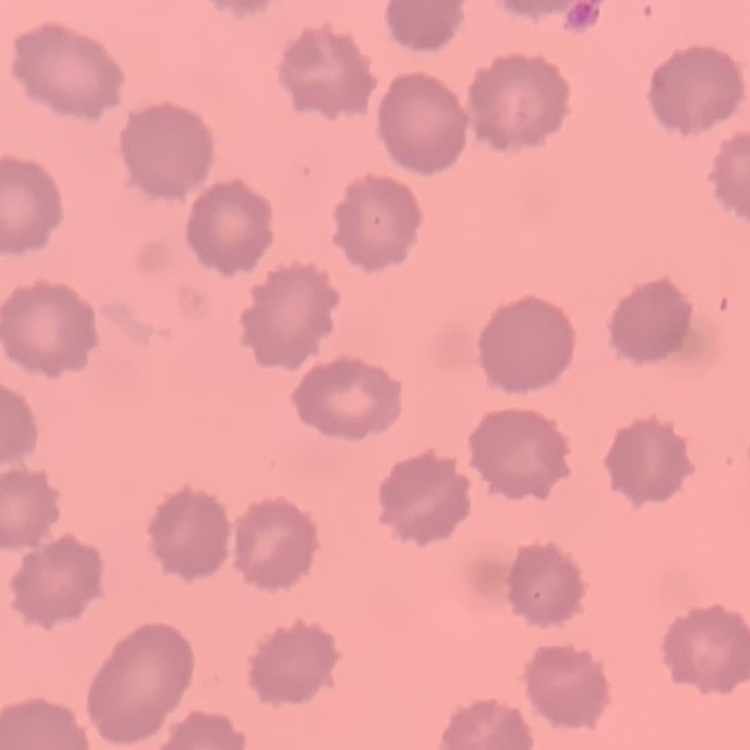
{
  "red_blood_cell_morphology": "no rouleaux formation",
  "image_type": "square crop of a larger photomicrograph",
  "stain": "Field's or Giemsa",
  "preparation": "thin peripheral smear"
}